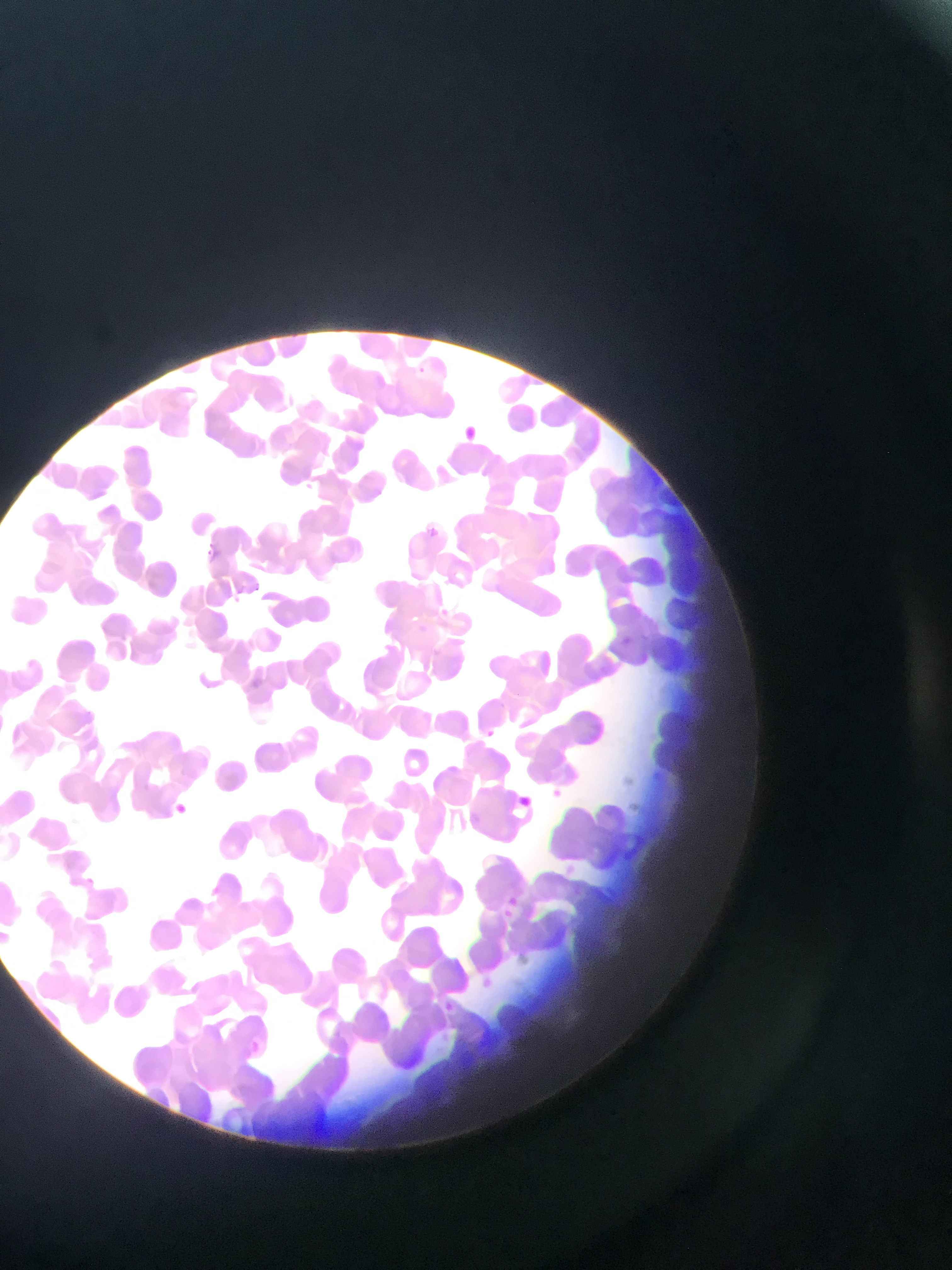
Approximate bounding boxes as left top right bottom in pixels.
Summary:
  - Malaria parasite locations: 299 469 323 501; 200 534 240 571; 228 589 251 623; 621 630 637 653; 480 721 492 740; 548 785 561 799; 521 790 533 814; 169 800 192 820; 501 887 524 910; 492 903 534 927; 490 970 508 999; 439 998 459 1015; 250 1037 266 1051
  - Capture: mobile-phone photograph through a microscope
  - Field of view: single
  - Country: Ghana
  - Preparation: thin blood smear
  - Image size: 952×1270 pixels